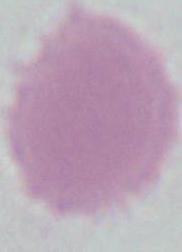

1000x magnification. An erythrocyte is seen. Photomicrograph.